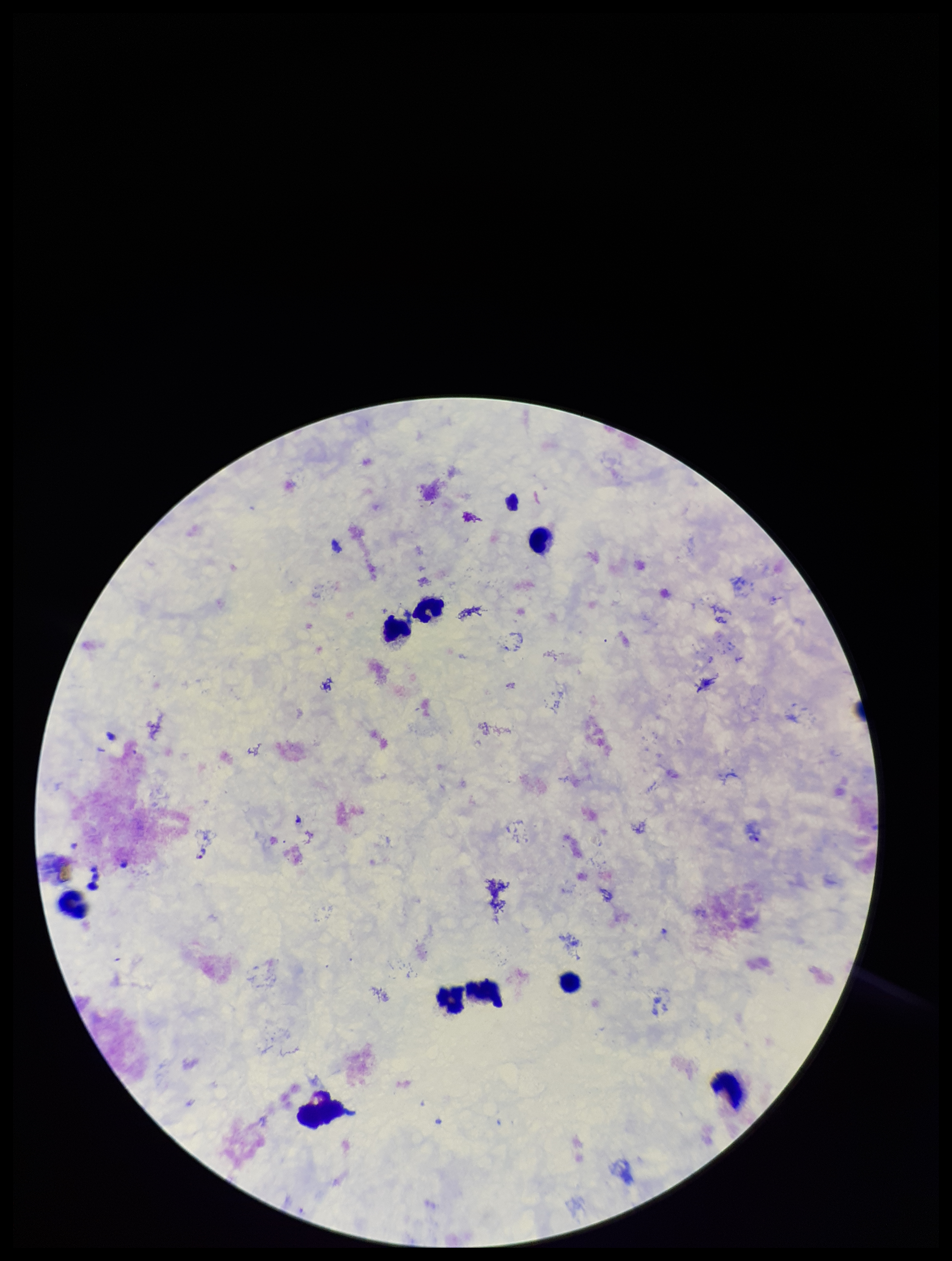
Photographed through the microscope eyepiece with a smartphone camera. Image is 952×1261 pixels. Patient malaria status: positive. Species reported for this patient: Plasmodium falciparum. Plasmodium parasites: detected. Stained with Giemsa. Preparation: thick. Single field of view. Leukocyte count: 9. Parasite count: 1.